Identify the cell.
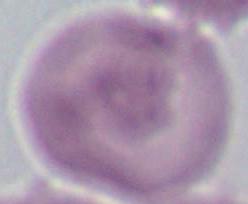
This is an erythrocyte.

Micrograph. 1000x magnification.